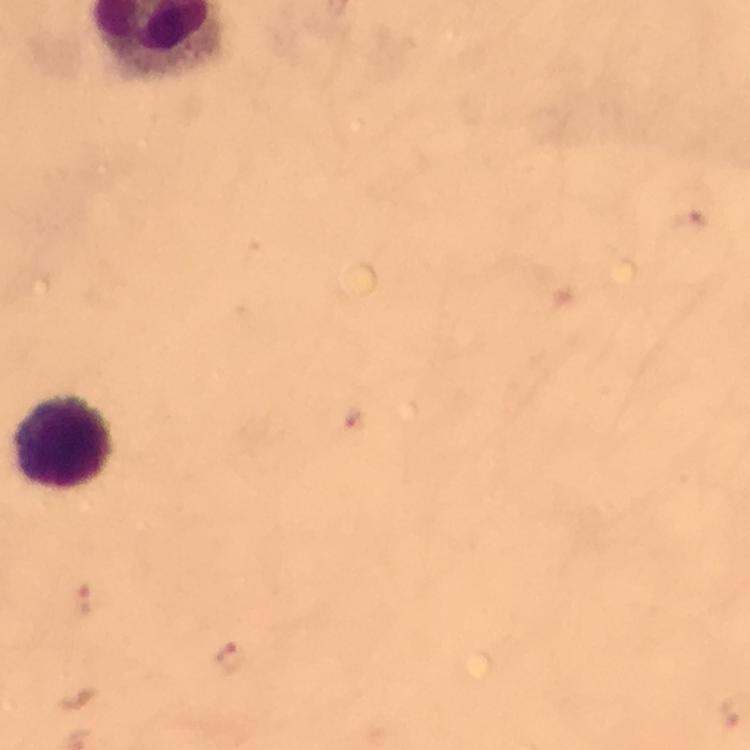
context = from a diagnostic examination for malaria
magnification = 100x
cropped from = one field of view
preparation = thick smear
capture = smartphone camera through the microscope
immersion oil = used
image size = 750×750 pixels
stain = Giemsa
leukocyte locations = approximate centers as (x, y) in pixels: (64, 442)
malaria parasite locations = approximate centers as (x, y) in pixels: (354, 421), (85, 599), (231, 656)